Give the position of every Plasmodium parasite and every leukocyte.
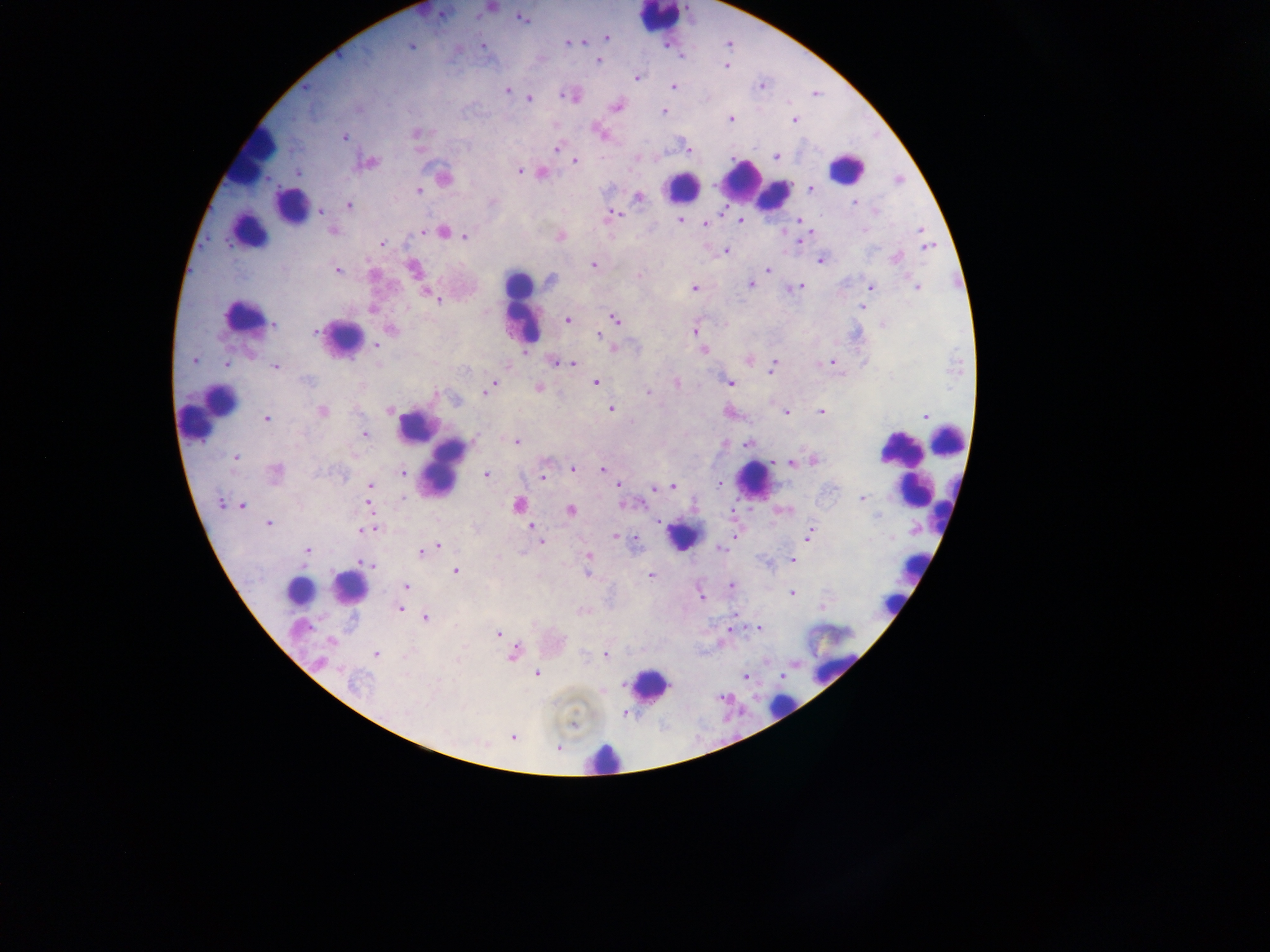

Approximate centers as x y in pixels.
Plasmodium parasites: 522 19; 606 37; 579 42; 567 43; 410 46; 483 47; 598 61; 726 65; 636 78; 673 86; 761 86; 507 90; 566 95; 529 98; 616 107; 664 111; 731 119; 794 119; 599 132; 416 133; 344 137; 556 148; 686 149; 638 157; 776 157; 575 161; 368 163; 519 172; 299 173; 543 173; 444 178; 810 188; 418 191; 638 197; 854 203; 349 205; 321 212; 876 212; 612 215; 740 220; 679 221; 799 221; 705 224; 921 229; 333 231; 423 231; 445 232; 810 232; 466 237; 559 237; 800 241; 382 243; 926 246; 725 252; 896 258; 821 260; 594 265; 413 269; 768 270; 337 271; 639 275; 550 279; 750 285; 799 286; 694 287; 872 287; 918 287; 426 293; 439 301; 862 307; 372 309; 615 318; 567 320; 274 324; 884 324; 391 330; 695 330; 315 332; 599 335; 376 345; 703 350; 192 360; 555 361; 750 361; 563 363; 572 363; 829 363; 226 364; 276 367; 773 367; 307 381; 596 383; 677 383; 729 383; 491 388; 538 388; 487 391; 648 392; 611 410; 322 411; 389 411; 821 412; 786 413; 925 416; 267 419; 365 435; 517 442; 747 444; 235 458; 814 460; 793 462; 573 468; 275 470; 603 470; 402 474; 486 475; 543 476; 719 483; 370 485; 619 486; 672 486; 656 488; 402 498; 861 499; 221 502; 367 502; 519 504; 634 505; 243 506; 571 511; 268 523; 531 527; 372 528; 364 530; 810 535; 616 538; 541 542; 438 546; 434 547; 721 548; 307 550; 421 553; 589 556; 792 560; 367 563; 455 571; 587 573; 650 576; 731 584; 405 587; 792 593; 700 596; 400 608; 426 618; 758 627; 499 633; 330 641; 376 653; 513 654; 605 655; 536 674; 745 676; 354 684; 573 725; 511 736; 557 748.
Leukocytes: 659 17; 251 157; 846 168; 743 178; 681 186; 774 195; 293 204; 248 231; 521 307; 243 316; 344 338; 207 410; 416 426; 947 440; 898 447; 445 467; 754 481; 913 492; 682 536; 915 566; 350 588; 298 591; 892 603; 835 649; 650 685; 780 707; 603 757.

Sample from Ghana. Thick blood film. Image is 1270×952 pixels. Photographed through a microscope with a mobile-phone camera. Single field of view.